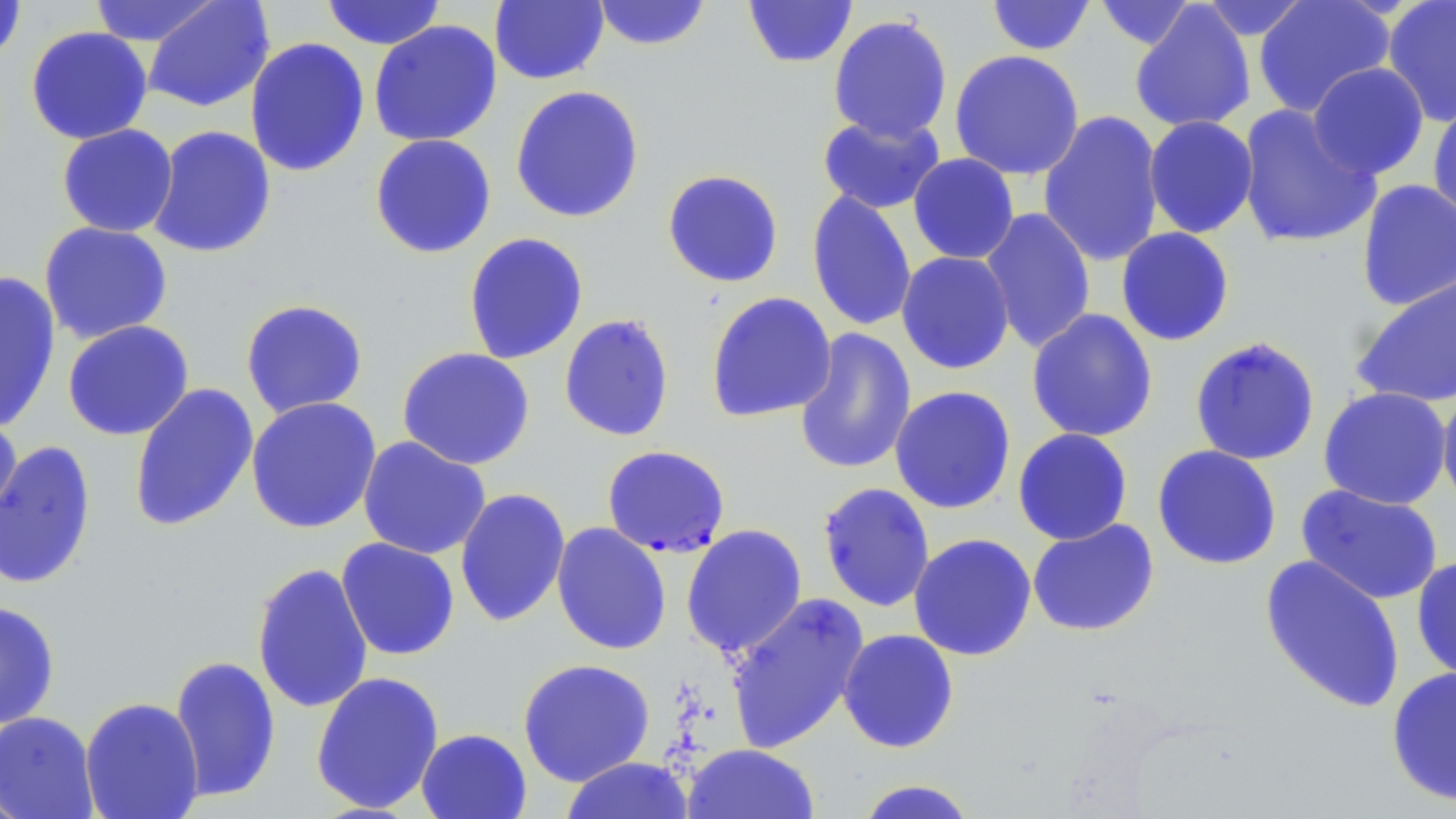
Summary:
  - Coordinate format: approximate bounding boxes as [x1, y1, x2, y2] in pixels
  - Uninfected red blood cell locations: [88, 0, 224, 47], [320, 0, 447, 50], [490, 0, 609, 85], [591, 0, 712, 51], [742, 0, 858, 69], [985, 0, 1097, 56], [1092, 0, 1198, 52], [1196, 0, 1313, 42], [1253, 0, 1396, 118], [1381, 0, 1456, 127], [0, 1, 28, 66], [143, 1, 274, 113], [1130, 2, 1256, 133], [827, 13, 953, 144], [368, 20, 502, 147], [25, 25, 153, 145], [244, 37, 370, 177], [948, 49, 1085, 180], [1307, 62, 1430, 180], [510, 85, 645, 223], [1426, 95, 1456, 225], [1236, 104, 1381, 250], [1038, 110, 1165, 267], [816, 113, 946, 215], [1143, 115, 1259, 239], [56, 123, 179, 238], [148, 125, 277, 259], [369, 134, 497, 258], [907, 153, 1020, 265], [661, 169, 785, 289], [1356, 179, 1456, 311], [806, 188, 917, 333], [979, 206, 1096, 354], [38, 221, 174, 345], [1115, 227, 1235, 347], [463, 232, 589, 365], [896, 251, 1015, 375], [0, 271, 61, 433], [1348, 271, 1456, 410], [705, 291, 837, 423], [239, 299, 369, 419], [1026, 308, 1159, 442], [558, 314, 675, 442], [62, 320, 194, 441], [794, 327, 917, 476], [1189, 336, 1321, 465], [396, 346, 536, 470], [128, 383, 259, 532], [1436, 384, 1456, 513], [889, 385, 1017, 515], [1317, 386, 1452, 510], [245, 396, 382, 534], [0, 415, 23, 537], [1012, 428, 1133, 545], [357, 436, 491, 559], [0, 439, 97, 589], [1152, 444, 1282, 570], [817, 482, 936, 612], [1296, 484, 1444, 605], [454, 487, 571, 628], [1027, 518, 1160, 637], [551, 522, 671, 656], [680, 523, 808, 658], [908, 532, 1037, 661], [336, 537, 460, 661], [1259, 553, 1406, 714], [1411, 555, 1456, 686], [251, 562, 374, 714], [725, 592, 870, 753], [0, 600, 60, 730], [837, 628, 960, 753], [169, 654, 281, 804], [517, 658, 656, 786], [1385, 665, 1456, 807], [310, 670, 445, 814], [79, 696, 204, 819], [0, 711, 100, 819], [416, 727, 532, 818], [682, 744, 820, 819], [559, 756, 696, 818], [852, 778, 980, 819]
  - Plasmodium falciparum-infected red blood cell locations: [601, 445, 730, 558]
  - Slide-level diagnosis: Plasmodium falciparum
  - Image size: 1456×819 pixels
  - Preparation: thin blood film
  - Stain: May-Grünwald-Giemsa
  - Modality: optical microscopy
  - Field of view: one of a larger specimen
  - Magnification: 1000x